Assess the morphology of the erythrocytes.
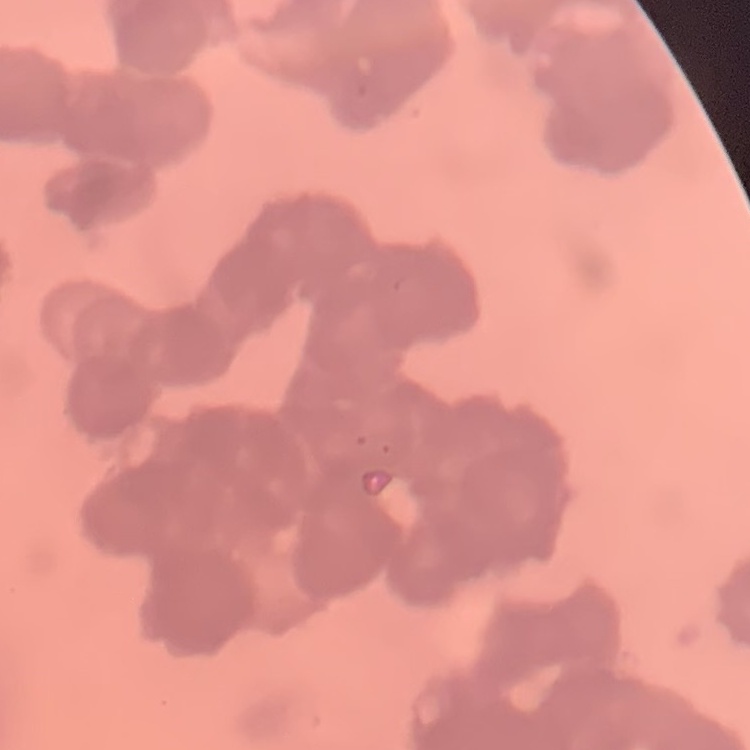
Rouleaux formation.

Summary:
  - Preparation: thin blood smear
  - Stain: Field's or Giemsa
  - Image type: one tile cut from a larger photomicrograph